Outline each blood parasite and name the species.
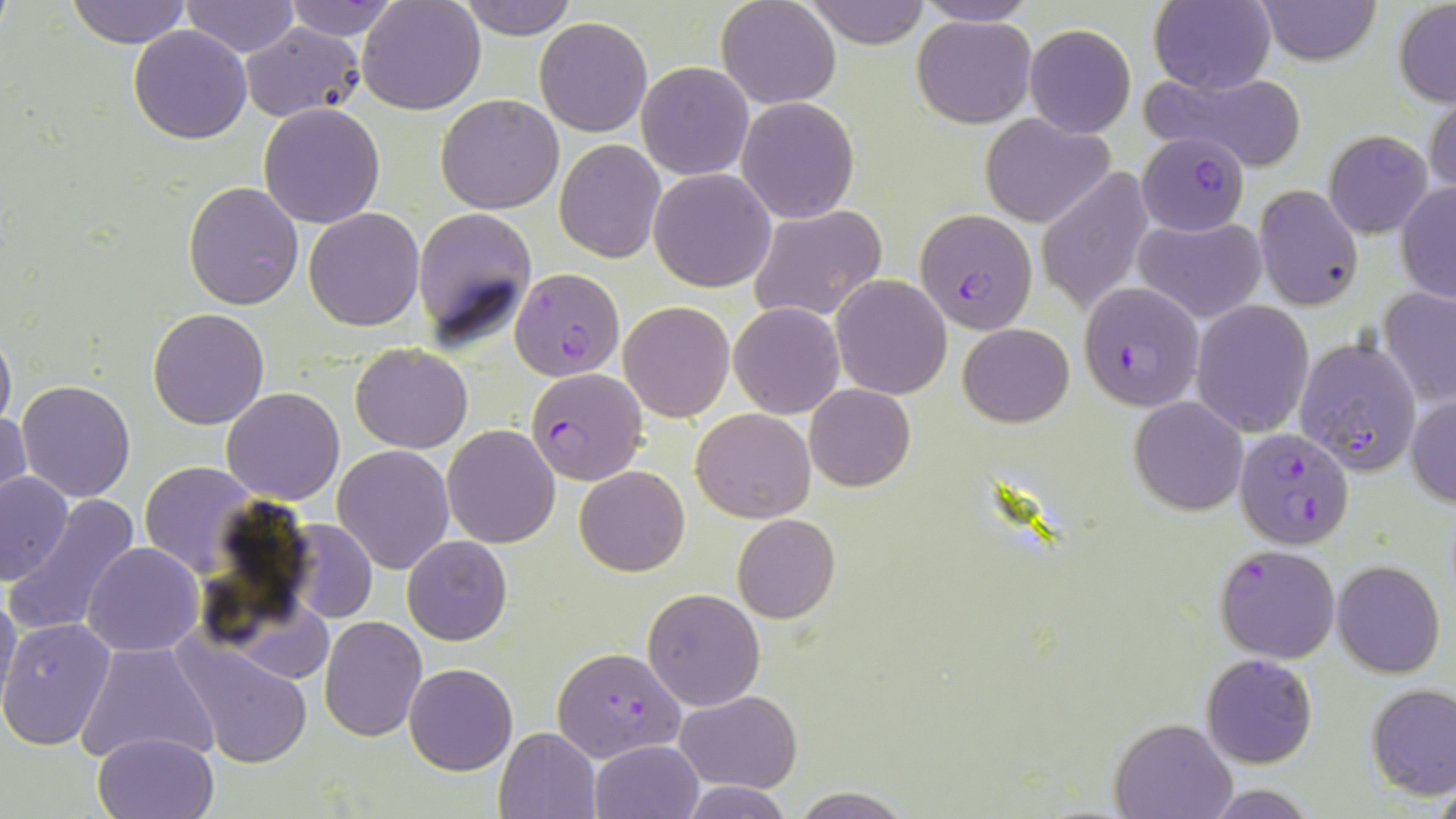
Approximate bounding boxes as [x1, y1, x2, y2] in pixels.
Plasmodium falciparum-infected red blood cells: [1138, 133, 1252, 236], [916, 209, 1039, 334], [510, 268, 625, 381], [1078, 282, 1204, 411], [1294, 336, 1421, 476], [525, 367, 648, 486], [1235, 429, 1354, 551], [1214, 543, 1341, 664], [553, 645, 686, 762].
No Plasmodium ovale, Plasmodium malariae, Plasmodium vivax, Babesia divergens, or Trypanosoma brucei observed.

Summary:
  - Uninfected red blood cell locations: [65, 0, 193, 48], [282, 0, 399, 41], [357, 0, 486, 114], [455, 0, 578, 40], [716, 0, 840, 109], [806, 0, 929, 46], [911, 0, 1041, 26], [1254, 0, 1382, 66], [182, 1, 299, 56], [1148, 1, 1276, 95], [1393, 1, 1456, 106], [912, 16, 1037, 128], [534, 17, 652, 137], [240, 23, 364, 121], [1023, 25, 1135, 137], [129, 26, 252, 145], [638, 62, 754, 180], [1142, 67, 1310, 169], [1426, 92, 1456, 201], [436, 94, 565, 213], [738, 97, 857, 222], [258, 103, 386, 228], [980, 113, 1114, 227], [1322, 130, 1433, 239], [556, 139, 665, 261], [1036, 167, 1154, 317], [650, 168, 775, 292], [184, 181, 304, 310], [1395, 181, 1456, 305], [1254, 184, 1364, 311], [748, 205, 887, 322], [412, 206, 537, 347], [304, 207, 425, 330], [1134, 215, 1267, 323], [831, 275, 951, 399], [1378, 286, 1456, 408], [1191, 299, 1314, 437], [620, 301, 735, 421], [730, 302, 844, 418], [149, 308, 269, 430], [958, 322, 1075, 428], [0, 327, 15, 434], [350, 343, 472, 453], [17, 380, 136, 502], [805, 384, 915, 492], [222, 387, 346, 504], [1407, 392, 1456, 507], [1129, 395, 1248, 515], [691, 407, 816, 523], [1, 408, 30, 516], [442, 425, 561, 549], [332, 445, 454, 573], [139, 461, 257, 576], [574, 466, 689, 577], [1, 470, 74, 586], [4, 492, 143, 642], [732, 514, 841, 624], [285, 519, 379, 624], [402, 536, 512, 646], [83, 542, 203, 656], [1332, 560, 1444, 678], [642, 588, 765, 710], [0, 589, 22, 715], [319, 616, 426, 740], [0, 619, 116, 749], [174, 635, 314, 769], [76, 640, 220, 767], [1201, 653, 1319, 769], [404, 663, 517, 775], [1366, 683, 1456, 800], [675, 689, 801, 793], [1109, 717, 1239, 818], [495, 726, 602, 818], [92, 730, 219, 819], [590, 739, 702, 818], [682, 781, 792, 817], [1201, 785, 1323, 817], [786, 788, 913, 818]
  - Slide-level diagnosis: Plasmodium falciparum
  - Field of view: one of a larger specimen
  - Image size: 1456×819 pixels
  - Preparation: thin blood film
  - Stain: May-Grünwald-Giemsa
  - Modality: light microscopy
  - Magnification: 1000x